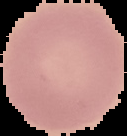
preparation = thin blood smear
image size = 127×136 pixels
image type = cell region segmented out of the field of view; surrounding area masked to black
result = negative for Plasmodium parasites